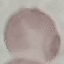
{
  "result": "no malaria parasites seen",
  "capture": "smartphone through the microscope eyepiece",
  "image_type": "automatically extracted cell patch, resized to 64 × 64 pixels",
  "stain": "Giemsa",
  "preparation": "thin blood smear"
}